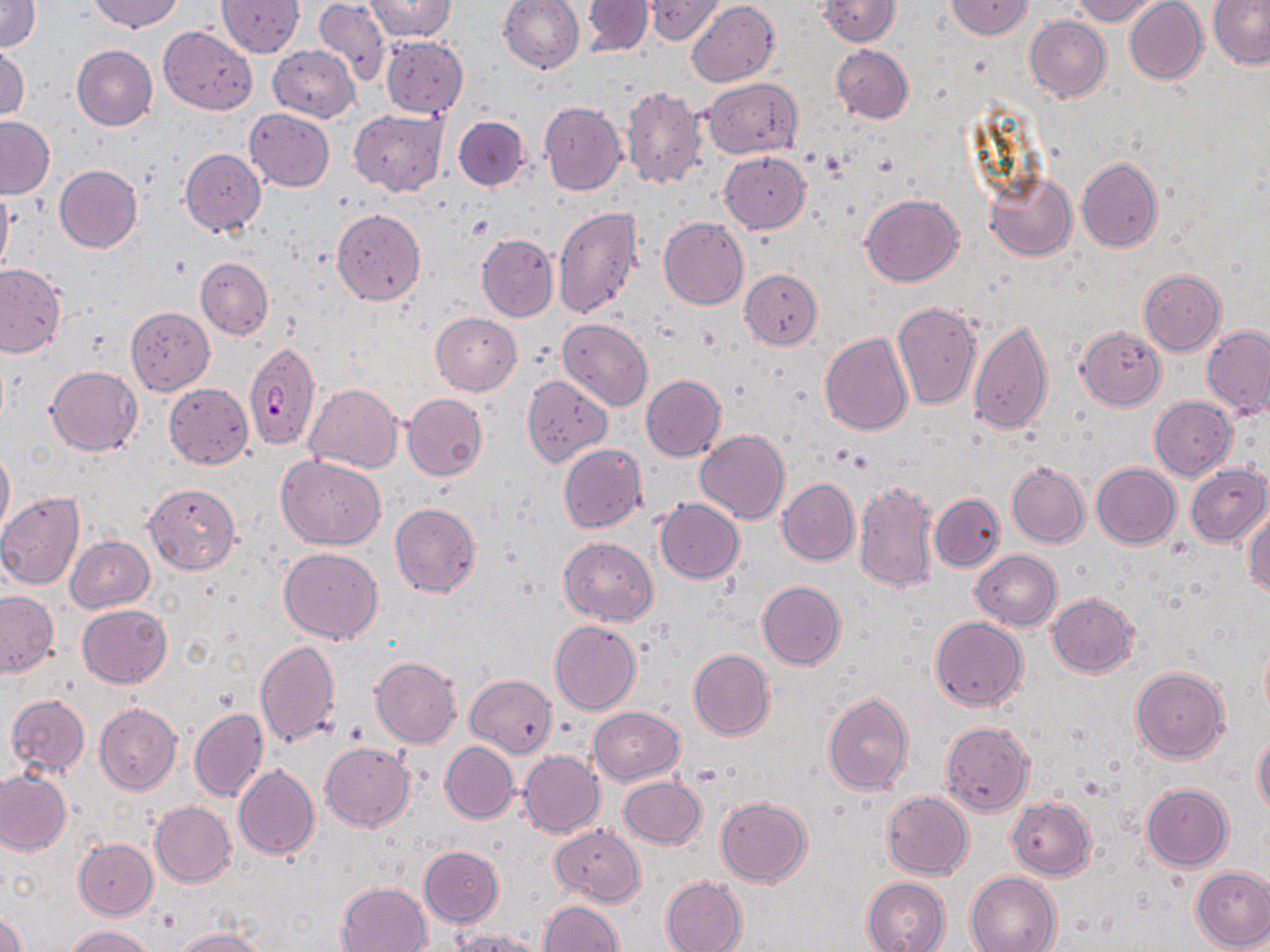
Summary:
  - Coordinate format: approximate bounding boxes as (x1,y1)-(x2,y2) corner pairs in pixels
  - Plasmodium falciparum-infected red blood cell locations: (244,341)-(319,452)
  - Uninfected red blood cell locations: (0,0)-(41,51), (90,0)-(183,33), (314,0)-(390,88), (365,0)-(456,41), (499,0)-(585,73), (583,0)-(655,56), (645,0)-(723,45), (817,0)-(900,46), (945,0)-(1032,38), (1071,0)-(1160,24), (1123,0)-(1208,85), (218,1)-(304,56), (688,1)-(779,88), (1208,2)-(1270,69), (1024,16)-(1111,102), (159,26)-(257,113), (381,36)-(469,117), (72,45)-(158,130), (268,45)-(359,123), (832,45)-(913,123), (1,46)-(29,121), (702,78)-(802,158), (620,85)-(706,190), (539,101)-(626,196), (244,108)-(335,191), (349,109)-(449,196), (0,116)-(53,198), (454,116)-(530,190), (179,149)-(265,236), (720,151)-(810,233), (1077,157)-(1162,252), (54,165)-(143,253), (984,172)-(1078,261), (1,186)-(13,281), (862,193)-(964,286), (552,205)-(643,319), (332,209)-(426,305), (658,217)-(748,310), (477,233)-(558,321), (196,258)-(274,339), (0,263)-(65,357), (741,269)-(822,349), (1138,269)-(1226,355), (892,301)-(981,410), (125,307)-(215,395), (423,308)-(509,472), (431,312)-(521,395), (558,318)-(653,411), (968,318)-(1053,436), (1201,324)-(1270,416), (1077,326)-(1165,409), (819,333)-(913,436), (46,365)-(142,455), (640,374)-(726,461), (522,376)-(612,465), (305,382)-(402,472), (164,383)-(253,469), (401,393)-(488,480), (1149,396)-(1238,480), (694,429)-(790,525), (559,443)-(646,534), (0,445)-(14,537), (278,456)-(384,550), (1007,462)-(1090,548), (1092,463)-(1180,549), (1185,464)-(1270,547), (778,477)-(859,566), (853,479)-(938,592), (145,482)-(241,575), (0,491)-(86,589), (931,493)-(1004,571), (655,498)-(744,583), (389,502)-(481,597), (1245,510)-(1270,598), (66,535)-(154,612), (558,537)-(658,625), (280,548)-(382,644), (971,550)-(1061,630), (758,581)-(846,669), (1,590)-(58,677), (1048,593)-(1139,677), (76,604)-(171,688), (931,616)-(1027,710), (549,620)-(641,715), (256,639)-(341,746), (689,649)-(775,740), (370,656)-(461,747), (1131,666)-(1229,763), (466,674)-(557,756), (823,692)-(913,794), (7,694)-(90,776), (96,703)-(181,795), (589,706)-(684,784), (188,707)-(267,802), (606,708)-(695,849), (941,721)-(1034,816), (1254,731)-(1270,819), (441,741)-(519,822), (320,742)-(415,831), (519,750)-(604,838), (233,765)-(319,861), (0,771)-(71,855), (619,776)-(706,848), (1142,783)-(1233,870), (881,791)-(973,879), (715,796)-(811,886), (1007,796)-(1096,879), (150,801)-(236,887), (549,824)-(646,906), (74,838)-(157,918), (419,845)-(504,927), (1191,867)-(1270,951), (965,871)-(1060,952), (661,875)-(747,952), (863,876)-(952,952), (337,881)-(432,951), (540,900)-(622,952), (0,908)-(25,952), (64,925)-(154,952), (171,928)-(266,951), (452,929)-(551,952)
  - Slide-level diagnosis: Plasmodium falciparum
  - Magnification: 1000x
  - Image size: 1270×952 pixels
  - Modality: light microscopy
  - Preparation: thin blood film
  - Stain: May-Grünwald-Giemsa
  - Field of view: single